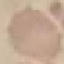

Malaria status: uninfected. Photographed with a smartphone camera at the microscope eyepiece. Thin smear of blood. Giemsa-stained preparation. Automatically extracted cell patch, resized to 64 × 64 pixels.